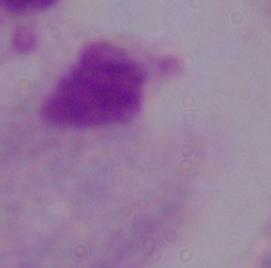

magnification: 1000x
identification: trichomonad
modality: photomicrograph